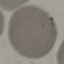

malaria_status: uninfected
capture: smartphone through the microscope eyepiece
image_type: automatically extracted cell patch, resized to 64 × 64 pixels
stain: Giemsa
preparation: thin blood smear